State the preparation type.
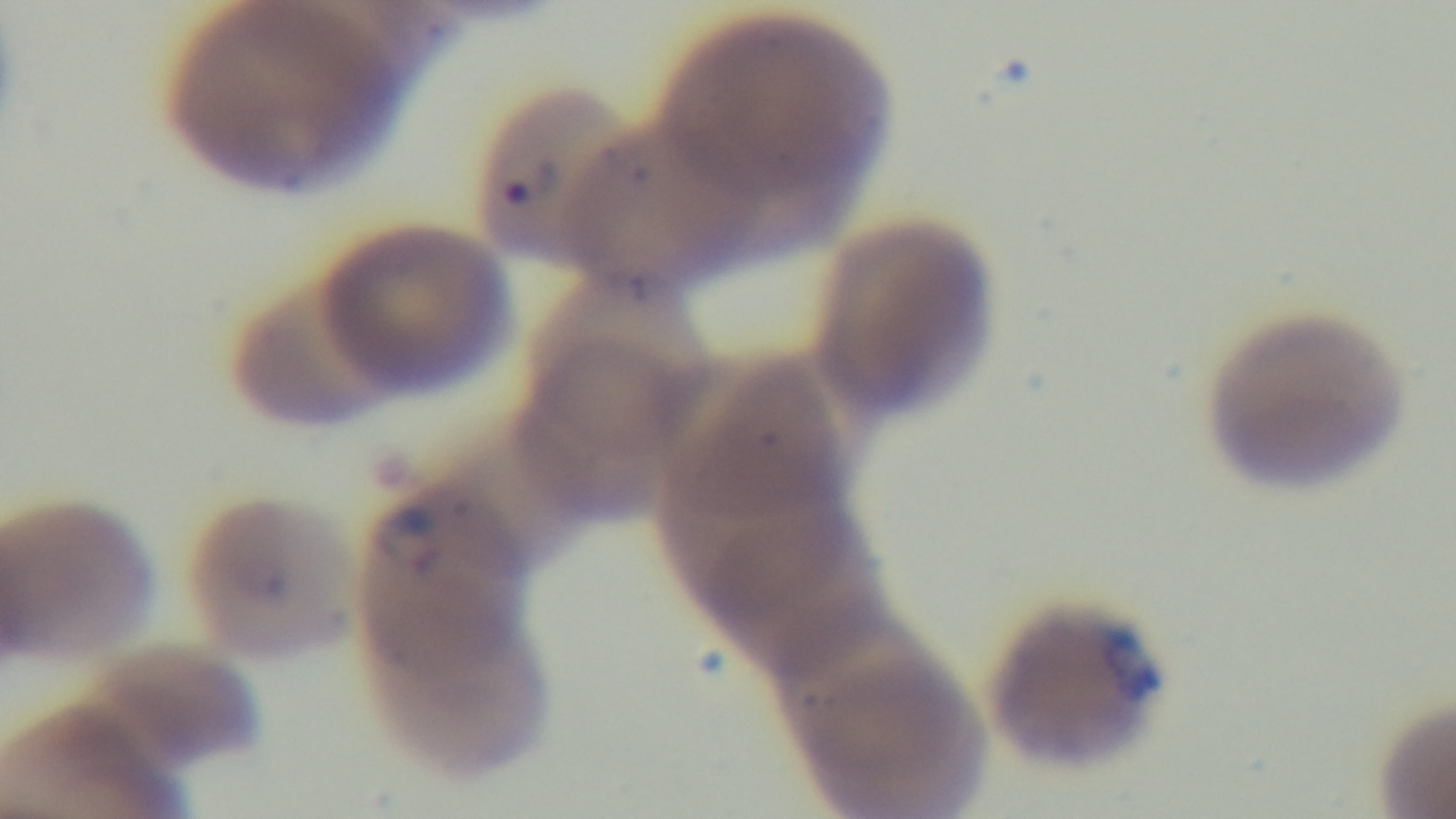

A thin smear.

Summary:
  - Capture: mounted 4K digital camera
  - Malaria status: infected
  - Modality: light microscopy
  - Field of view: single
  - Objective: 100x oil immersion
  - Stain: Giemsa